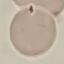

Summary:
  - Result: no malaria parasites seen
  - Preparation: thin blood film
  - Image type: cell patch, automatically extracted from a larger field of view and resized to 64 × 64 pixels
  - Stain: Giemsa
  - Capture: smartphone camera at the microscope eyepiece